Report the malaria status of this cell.
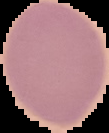

It is uninfected.

Image is 109×133 pixels. The area outside the segmented cell region is set to black. From a thin blood smear.